Assess the morphology of the red blood cells.
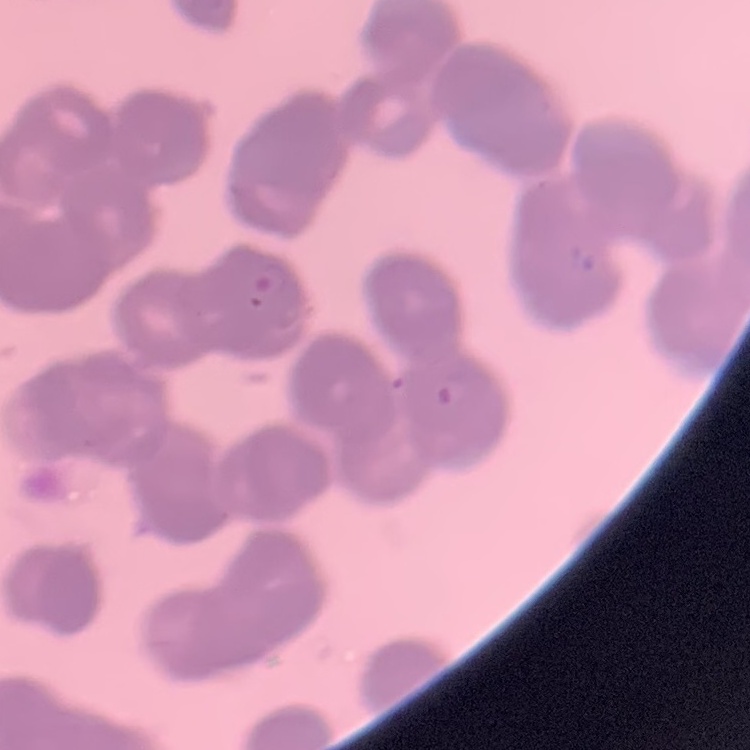

Rouleaux formation.

Summary:
  - Preparation: thin blood smear
  - Stain: Field's or Giemsa
  - Image type: square crop of a larger photomicrograph